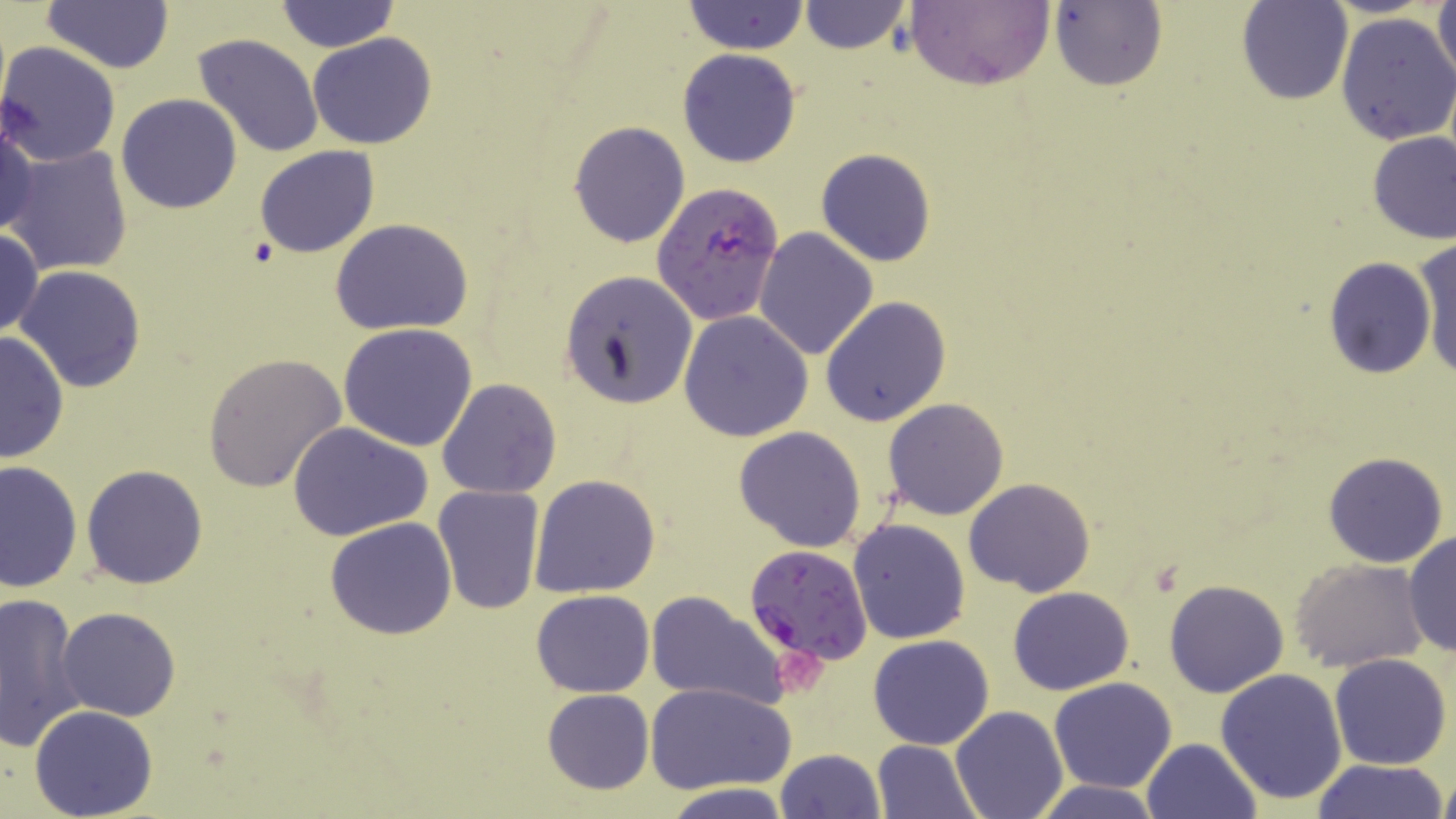

Approximate bounding boxes as (x1, y1, x2, y2) in pixels. Platelet locations: (774, 651, 833, 696). Plasmodium falciparum-infected red blood cell locations: (651, 182, 785, 327), (744, 543, 873, 665). Uninfected red blood cell locations: (273, 0, 399, 53), (1430, 0, 1456, 94), (41, 1, 174, 72), (683, 1, 809, 54), (797, 1, 911, 54), (903, 1, 1053, 90), (1237, 1, 1353, 106), (1049, 2, 1168, 91), (1335, 11, 1456, 146), (307, 32, 437, 149), (193, 33, 324, 160), (0, 41, 122, 168), (678, 48, 801, 168), (116, 93, 242, 214), (0, 115, 37, 242), (569, 122, 689, 249), (1367, 131, 1455, 244), (4, 145, 134, 277), (254, 145, 379, 258), (816, 148, 938, 267), (329, 217, 473, 336), (753, 226, 878, 360), (0, 229, 44, 341), (1413, 233, 1456, 381), (1322, 256, 1436, 379), (15, 267, 146, 392), (560, 270, 697, 408), (820, 296, 950, 428), (679, 311, 812, 441), (337, 323, 479, 450), (0, 329, 69, 464), (202, 353, 347, 492), (437, 379, 562, 500), (882, 398, 1010, 520), (287, 419, 432, 541), (733, 426, 865, 552), (1322, 452, 1450, 568), (0, 459, 82, 595), (81, 464, 208, 588), (530, 474, 660, 597), (963, 478, 1095, 598), (432, 485, 545, 614), (325, 517, 457, 640), (846, 517, 971, 646), (1403, 530, 1456, 660), (1291, 559, 1428, 674), (1163, 579, 1290, 698), (1009, 587, 1133, 695), (530, 590, 655, 696), (645, 592, 788, 711), (0, 593, 87, 752), (56, 606, 181, 721), (869, 635, 995, 750), (1330, 654, 1452, 770), (1215, 668, 1349, 805), (1048, 677, 1178, 794), (645, 682, 796, 796), (541, 688, 654, 794), (950, 704, 1068, 819), (29, 705, 157, 818), (1141, 738, 1262, 819), (873, 740, 983, 819), (776, 748, 884, 818), (1308, 759, 1451, 819), (1438, 769, 1456, 819), (1034, 780, 1164, 818), (658, 784, 795, 818). Slide-level diagnosis: Plasmodium falciparum. One field of a larger specimen. Optical microscopy. Image is 1456×819 pixels. 1000x magnification. Thin blood smear. May-Grünwald-Giemsa-stained preparation.